Report the malaria status of this cell.
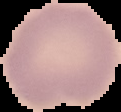

It is uninfected.

{
  "preparation": "thin blood smear",
  "image_type": "segmented cell region with the area outside set to black",
  "image_size": "121×112 pixels"
}